Name the parasite shown.
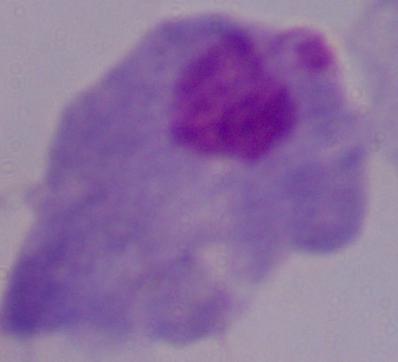
A trichomonad.

1000x magnification. Photomicrograph.